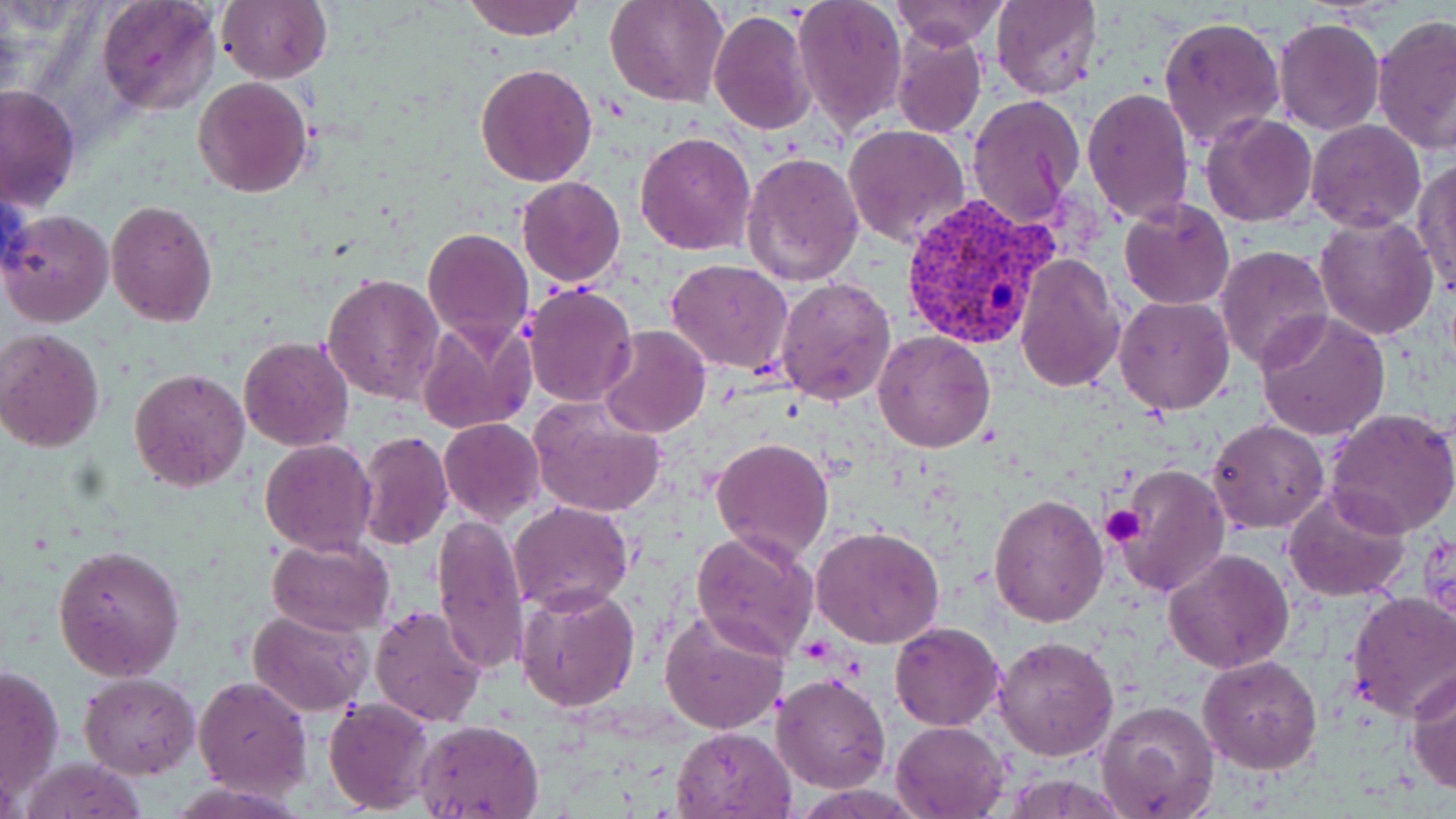

{
  "slide_level_diagnosis": "Plasmodium vivax",
  "magnification": "1000x",
  "plasmodium_vivax_infected_red_blood_cell_locations": "approximate bounding boxes as (x1, y1, x2, y2) in pixels: (897, 193, 1060, 351)",
  "stain": "May-Grünwald-Giemsa",
  "modality": "light microscopy",
  "platelet_locations": "approximate bounding boxes as (x1, y1, x2, y2) in pixels: (1101, 504, 1146, 547)",
  "uninfected_red_blood_cell_locations": "approximate bounding boxes as (x1, y1, x2, y2) in pixels: (216, 0, 332, 84), (462, 0, 583, 41), (607, 0, 728, 106), (791, 0, 906, 131), (891, 1, 1009, 48), (991, 1, 1102, 98), (95, 2, 220, 116), (708, 7, 816, 136), (1373, 14, 1455, 159), (1159, 16, 1286, 149), (1273, 18, 1386, 135), (890, 27, 987, 139), (476, 63, 598, 186), (194, 77, 312, 198), (0, 82, 81, 213), (1081, 88, 1195, 226), (967, 94, 1086, 228), (1200, 113, 1319, 227), (1306, 120, 1427, 232), (842, 123, 970, 250), (635, 132, 755, 256), (741, 151, 865, 288), (1411, 158, 1456, 295), (516, 176, 626, 288), (1120, 197, 1234, 310), (105, 201, 217, 327), (1, 208, 115, 327), (1314, 213, 1439, 339), (423, 227, 533, 346), (1215, 244, 1335, 371), (1014, 254, 1125, 394), (665, 258, 794, 375), (322, 273, 444, 404), (774, 276, 896, 406), (521, 284, 636, 408), (1114, 296, 1235, 415), (1256, 310, 1390, 443), (415, 315, 536, 435), (597, 326, 709, 438), (0, 329, 105, 453), (873, 330, 997, 452), (239, 336, 354, 452), (129, 368, 251, 492), (528, 394, 668, 518), (1327, 407, 1456, 538), (439, 418, 546, 526), (1206, 419, 1328, 534), (356, 431, 454, 550), (711, 435, 834, 561), (259, 438, 378, 555), (1115, 461, 1230, 598), (1283, 486, 1410, 604), (988, 494, 1109, 627), (510, 502, 634, 614), (431, 511, 529, 677), (811, 526, 945, 649), (691, 529, 819, 662), (267, 538, 396, 637), (53, 545, 185, 683), (1163, 549, 1295, 674), (513, 586, 641, 714), (1345, 590, 1456, 722), (370, 604, 487, 729), (657, 608, 789, 736), (247, 609, 372, 715), (890, 623, 1004, 730), (991, 633, 1119, 760), (1198, 654, 1324, 774), (0, 663, 65, 803), (1405, 668, 1456, 795), (771, 671, 891, 793), (78, 673, 201, 778), (191, 674, 314, 799), (323, 698, 438, 815), (1094, 700, 1221, 818), (416, 718, 545, 819), (892, 720, 1010, 818), (672, 726, 797, 818), (20, 756, 148, 818)",
  "preparation": "thin blood film",
  "field_of_view": "one of a larger specimen",
  "image_size": "1456×819 pixels"
}